Outline each Plasmodium falciparum parasite and classify it by life-cycle stage.
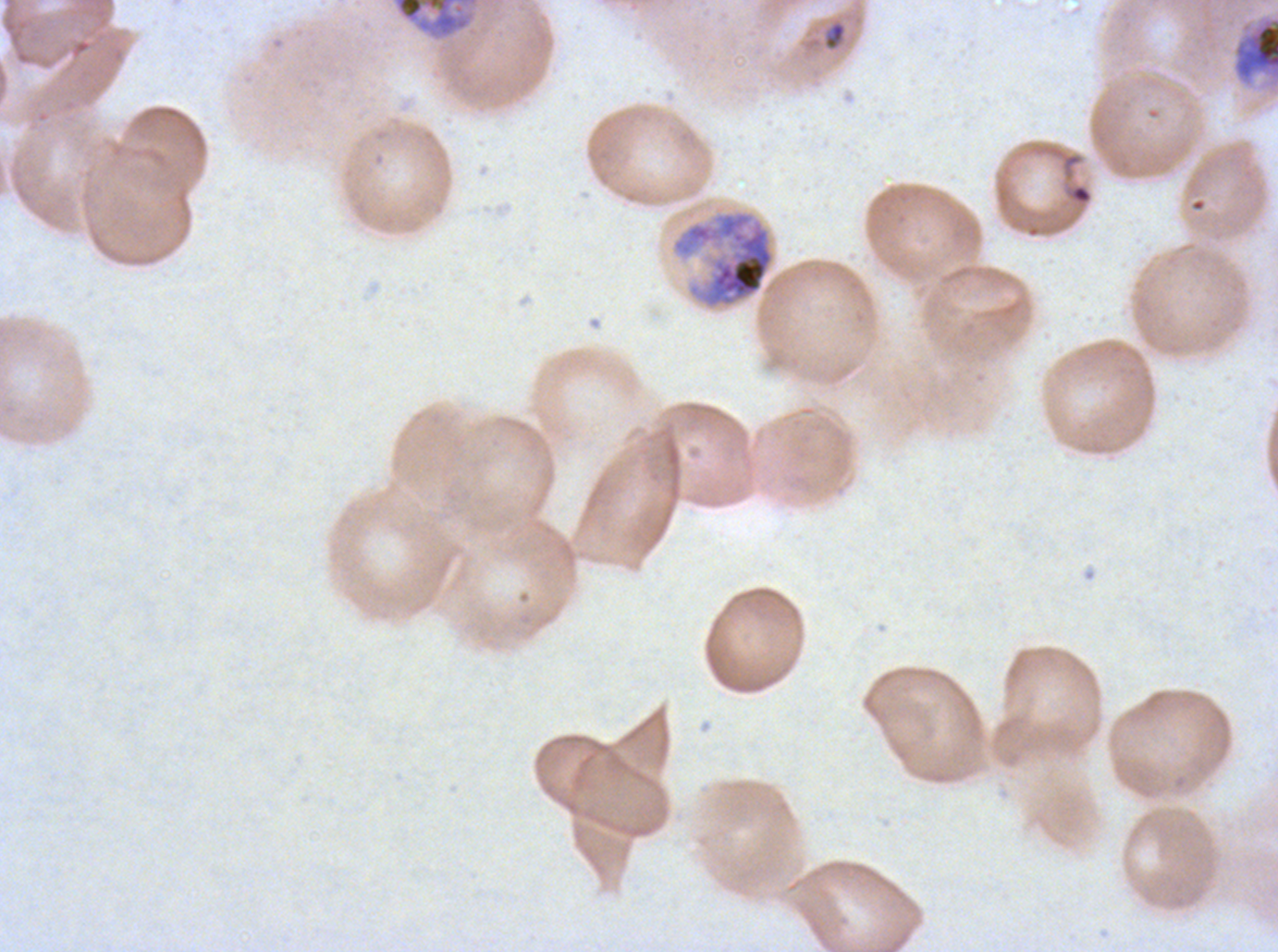

Approximate bounding boxes as [x1, y1, x2, y2] in pixels.
Rings: [1070, 184, 1092, 204].
Late-ring/early-trophozoite forms: [824, 21, 846, 49].
Late trophozoites: [391, 0, 479, 40].
Early schizonts: [1230, 12, 1277, 95], [670, 209, 776, 310].
No mid trophozoites, late schizonts, segmenters, or gametocytes observed.

One sub-image of a larger composite. Life-cycle stages observed: ring, late-ring/early-trophozoite, late trophozoite, early schizont. Giemsa-stained preparation. Image is 1278×952 pixels. Plasmodium falciparum cultured ex vivo for 24 to 48 hours, from a patient in The Gambia. Thin blood film.